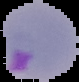
Summary:
  - Preparation: thin blood smear
  - Malaria status: parasitized
  - Image size: 79×82 pixels
  - Image type: segmented cell region on a black background